Assess the morphology of the red blood cells.
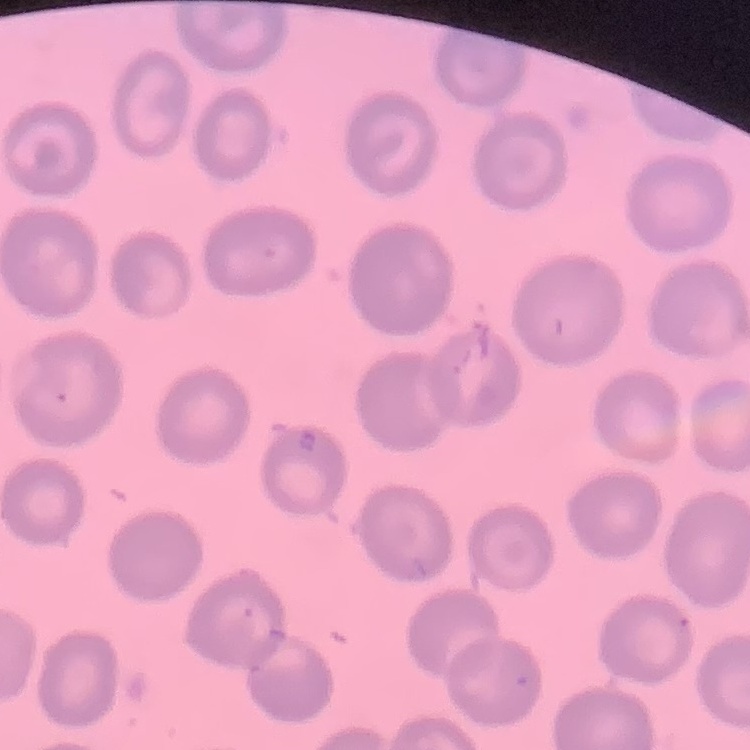

No rouleaux formation.

Thin blood film. Field's or Giemsa stain. Square crop of a larger photomicrograph.